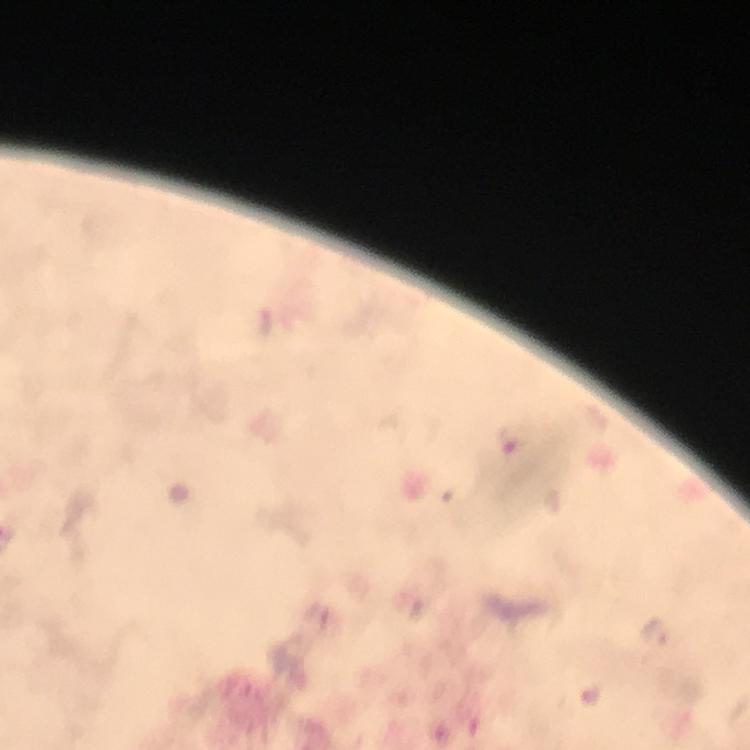

Approximate centers as {x, y} in pixels.
Summary:
  - Plasmodium parasite locations: {513, 438}, {653, 632}
  - Stain: Giemsa
  - Cropped from: a single field of view
  - Magnification: 100x
  - Context: from a malaria diagnostic workup
  - Preparation: thick blood film
  - Capture: smartphone mounted on the microscope
  - Immersion oil: applied
  - Image size: 750×750 pixels